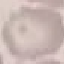
Malaria status: uninfected. Acquired by smartphone through the microscope eyepiece. Giemsa-stained preparation. Cell patch, automatically extracted from a larger field of view and resized to 64 × 64 pixels. Thin smear of blood.